Report the malaria status of this cell.
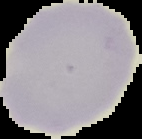

It is uninfected.

preparation: thin blood smear
image_type: cell region segmented out of the field of view; surrounding area masked to black
image_size: 142×139 pixels